Identify the parasite.
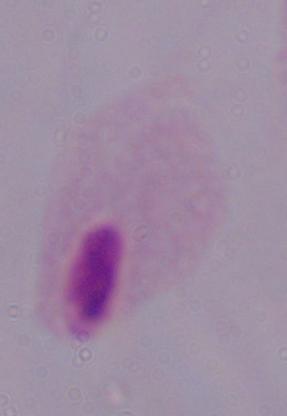

This is a trichomonad.

Photomicrograph. Captured at 1000x magnification.